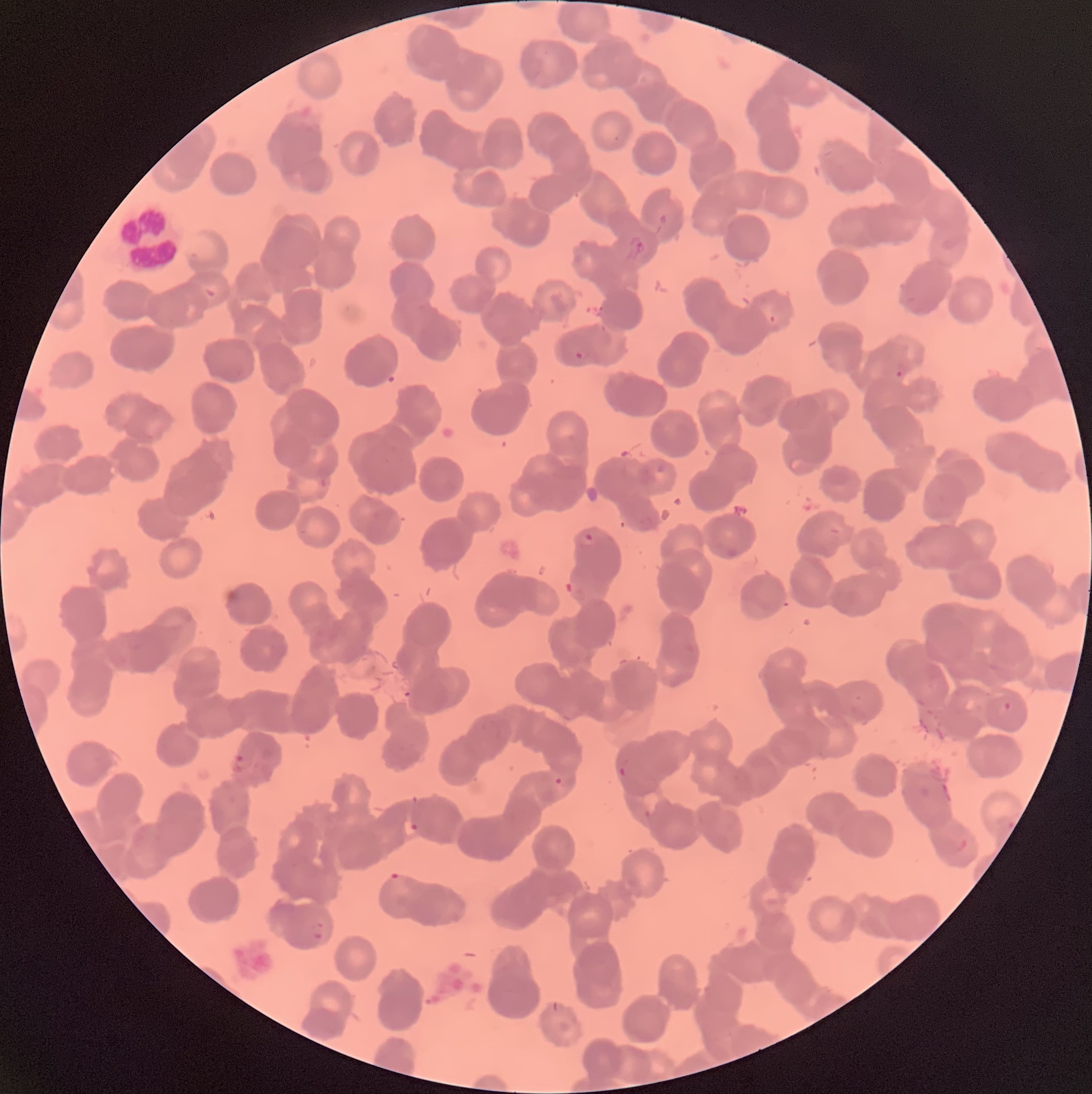

coordinate format = approximate bounding boxes as (x1,y1)-(x2,y2) corner pairs in pixels
Plasmodium parasite locations = (658,214)-(668,225), (626,236)-(645,260), (205,288)-(216,298), (769,315)-(776,324), (575,351)-(582,360), (896,362)-(909,378), (579,532)-(596,547), (1003,700)-(1012,711), (232,755)-(253,772), (618,765)-(627,777), (553,777)-(563,786), (643,809)-(653,819), (410,822)-(420,832), (388,871)-(402,883), (311,921)-(324,938)
white blood cell locations = (117,202)-(182,275)
red blood cell morphology = rouleaux formation
modality = light microscopy
preparation = thin blood smear
image size = 1092×1094 pixels